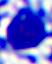
{
  "magnification": "400x",
  "modality": "micrograph",
  "identification": "leukocyte"
}